Name the parasite shown.
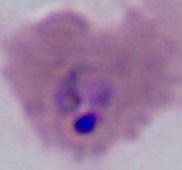
Plasmodium.

{
  "modality": "photomicrograph",
  "magnification": "400x or 1000x"
}